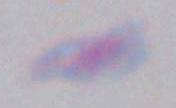

1000x magnification. Toxoplasma gondii is shown. Photomicrograph.